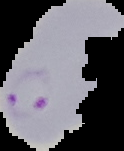 Image is 124×151 pixels. The area outside the segmented cell region is set to black. From a thin blood film. Malaria status: parasitized.